Name the parasite shown.
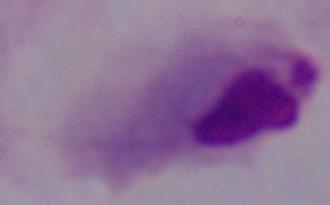
A trichomonad.

magnification = 1000x
modality = photomicrograph